State which parasite is depicted.
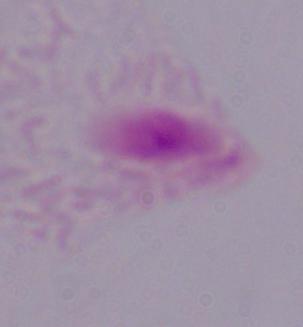

This is a trichomonad.

Summary:
  - Magnification: 1000x
  - Modality: micrograph